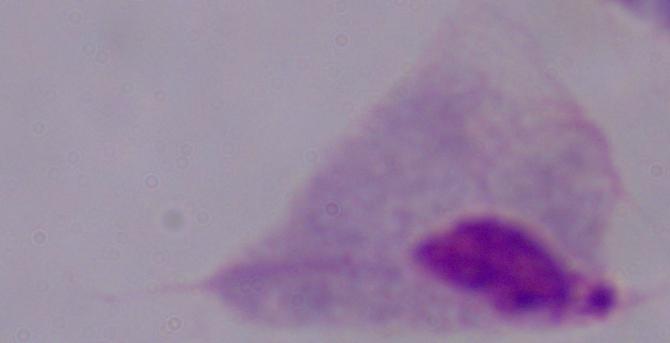 Captured at 1000x magnification. A trichomonad is shown. Micrograph.